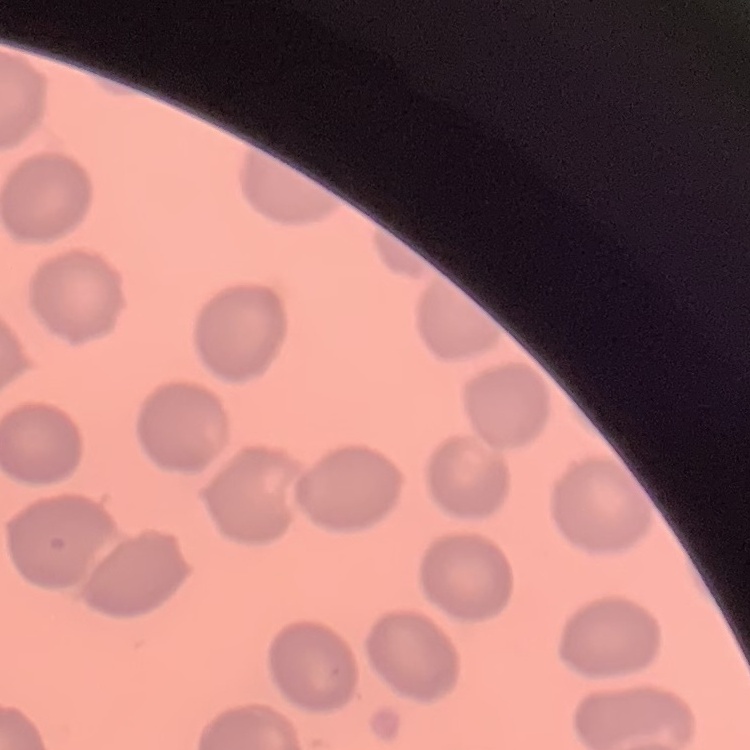
Summary:
  - Erythrocyte morphology: no rouleaux formation
  - Image type: square crop of a larger photomicrograph
  - Preparation: thin blood film
  - Stain: Field's or Giemsa